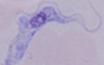

A trypanosome is seen. Photomicrograph. 1000x magnification.